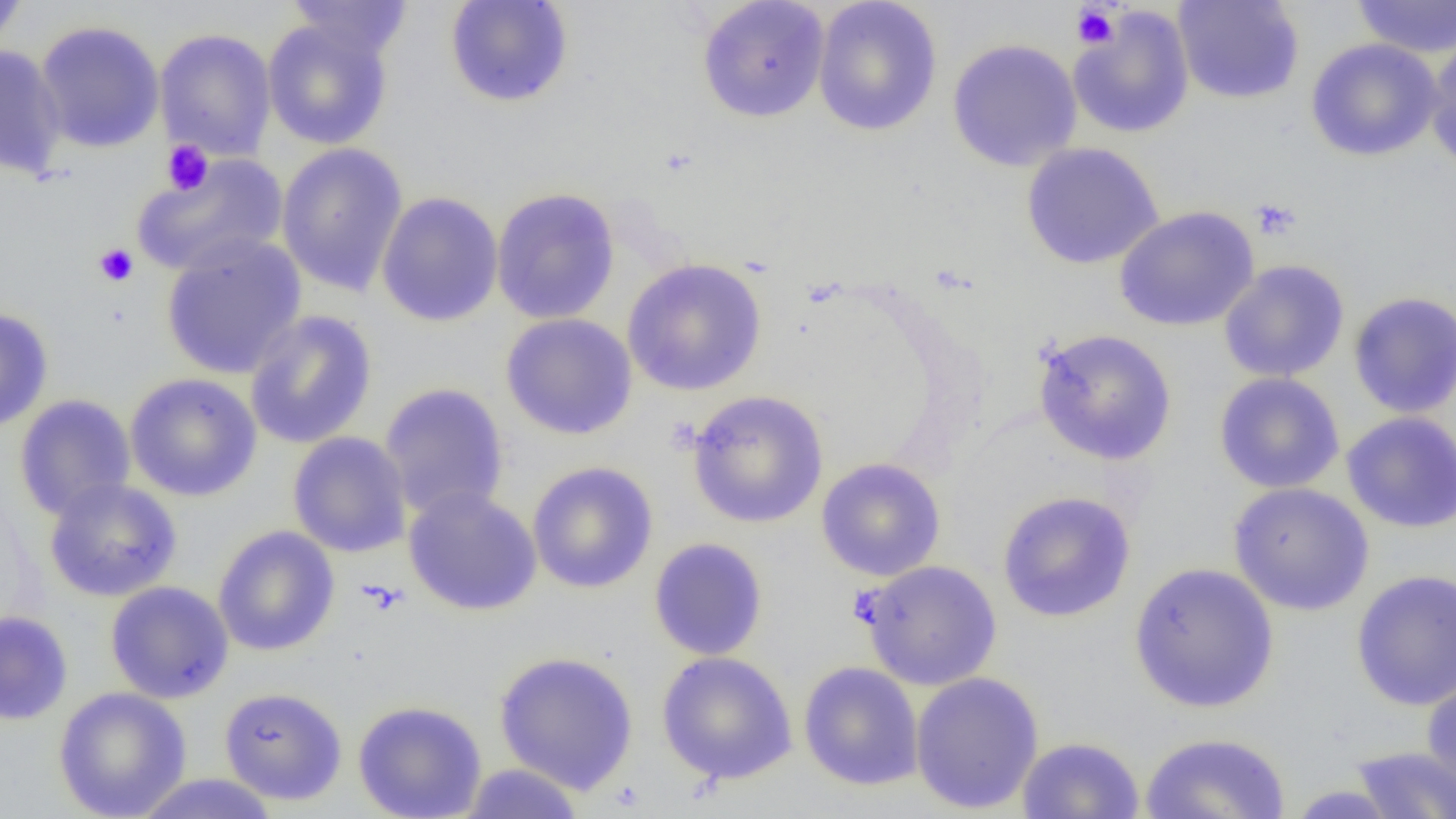
slide-level diagnosis = no evidence of blood parasites
platelet locations = approximate bounding boxes as [x1, y1, x2, y2] in pixels: [1071, 5, 1120, 50], [162, 140, 213, 195], [1249, 198, 1301, 240], [93, 243, 139, 287], [358, 579, 408, 616]
magnification = 1000x
image size = 1456×819 pixels
field of view = single
preparation = thin blood film
modality = optical microscopy
uninfected red blood cell locations = approximate bounding boxes as [x1, y1, x2, y2] in pixels: [0, 0, 28, 53], [285, 0, 413, 60], [444, 0, 574, 108], [696, 0, 830, 123], [1173, 0, 1304, 105], [1351, 0, 1456, 58], [812, 1, 942, 136], [1068, 7, 1195, 140], [262, 18, 394, 150], [34, 20, 165, 153], [155, 28, 276, 161], [1425, 34, 1456, 174], [946, 38, 1083, 172], [1305, 38, 1443, 162], [0, 45, 67, 180], [277, 142, 409, 296], [1020, 142, 1164, 270], [130, 153, 289, 278], [491, 187, 621, 325], [376, 192, 503, 327], [1113, 205, 1260, 332], [160, 236, 308, 380], [623, 259, 767, 396], [1218, 259, 1350, 383], [1347, 291, 1456, 419], [0, 306, 54, 432], [243, 309, 378, 450], [500, 312, 638, 440], [1033, 328, 1177, 466], [124, 372, 263, 502], [1213, 372, 1345, 494], [378, 382, 510, 521], [686, 390, 829, 528], [14, 394, 137, 521], [1341, 411, 1456, 534], [287, 431, 412, 558], [816, 457, 946, 581], [526, 461, 659, 594], [43, 477, 182, 601], [1227, 481, 1374, 616], [402, 486, 542, 616], [997, 490, 1136, 623], [212, 525, 340, 656], [648, 537, 768, 660], [858, 560, 1002, 690], [1128, 561, 1280, 713], [1351, 569, 1456, 711], [105, 580, 234, 704], [0, 610, 73, 725], [494, 650, 639, 795], [656, 651, 798, 785], [798, 661, 924, 791], [1421, 670, 1456, 796], [910, 671, 1045, 814], [53, 686, 192, 819], [219, 686, 348, 805], [353, 699, 487, 819], [1139, 731, 1292, 819], [1016, 736, 1145, 819], [1348, 746, 1456, 818], [458, 762, 587, 818], [130, 773, 281, 818], [1282, 784, 1405, 818]